Identify the cell.
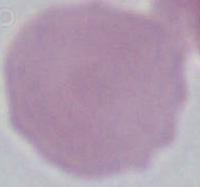

This is an erythrocyte.

Photomicrograph. 1000x magnification.